Locate every blood parasite and identify its species.
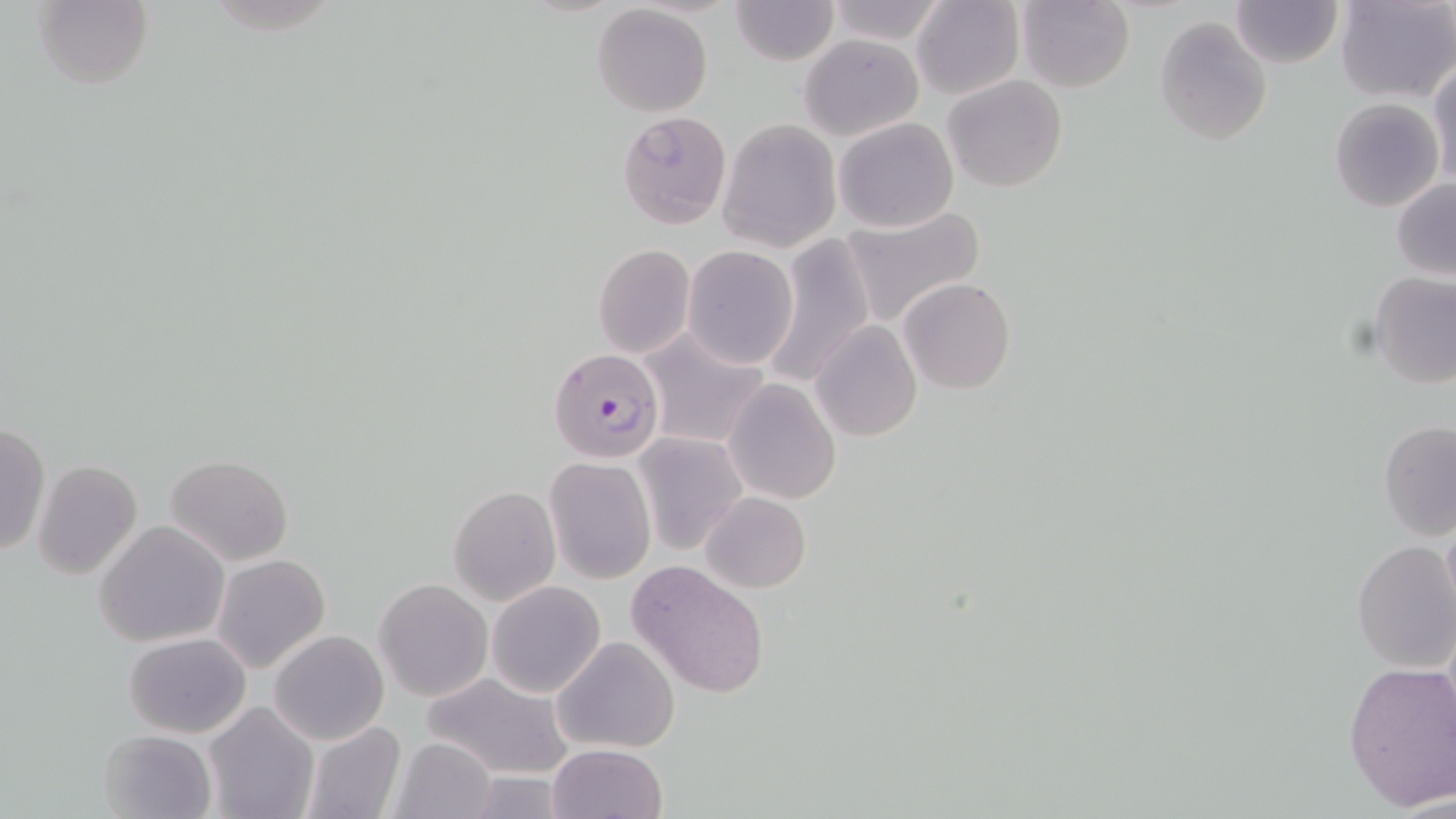
Approximate bounding boxes as (x1,y1)-(x2,y2) corner pairs in pixels.
Plasmodium falciparum-infected red blood cells: (549,346)-(666,465).
No Plasmodium ovale, Plasmodium malariae, Plasmodium vivax, Babesia divergens, or Trypanosoma brucei observed.

Uninfected red blood cell locations: (30,0)-(152,89), (731,0)-(838,66), (824,0)-(949,45), (911,0)-(1024,100), (1015,0)-(1135,91), (1335,0)-(1454,102), (1231,1)-(1342,69), (591,4)-(713,116), (1154,16)-(1271,145), (799,33)-(924,141), (1429,59)-(1456,189), (942,75)-(1069,192), (1330,98)-(1445,212), (617,110)-(732,228), (717,117)-(842,253), (833,117)-(959,233), (1392,178)-(1456,279), (838,205)-(986,328), (761,235)-(876,390), (592,244)-(695,359), (682,245)-(797,368), (1368,272)-(1455,388), (899,277)-(1017,394), (810,321)-(923,442), (635,328)-(770,449), (723,379)-(841,505), (1378,419)-(1456,541), (0,423)-(49,556), (632,433)-(747,555), (166,454)-(294,565), (544,457)-(655,583), (35,460)-(142,579), (448,484)-(560,605), (701,491)-(810,592), (1441,510)-(1456,631), (95,520)-(230,648), (1351,540)-(1455,672), (212,554)-(332,674), (625,559)-(772,701), (374,579)-(492,701), (486,581)-(607,699), (269,629)-(389,745), (123,632)-(251,739), (551,636)-(680,754), (1342,660)-(1456,810), (422,673)-(575,779), (203,701)-(318,819), (300,721)-(407,819), (98,728)-(217,819), (387,735)-(499,819), (547,743)-(667,819). Slide-level diagnosis: Plasmodium falciparum. Image is 1456×819 pixels. 1000x magnification. Light microscopy. Thin blood film. One field of a larger specimen. May-Grünwald-Giemsa stain.